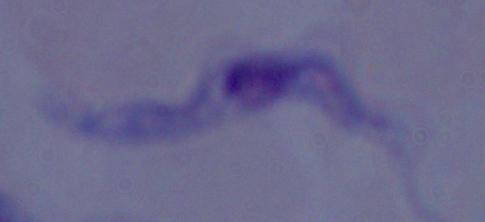

modality: photomicrograph
magnification: 1000x
identification: trypanosome